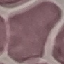
Summary:
  - Result: no malaria parasites seen
  - Capture: smartphone through the microscope eyepiece
  - Preparation: thin smear
  - Stain: Giemsa
  - Image type: automatically extracted cell patch, resized to 64 × 64 pixels